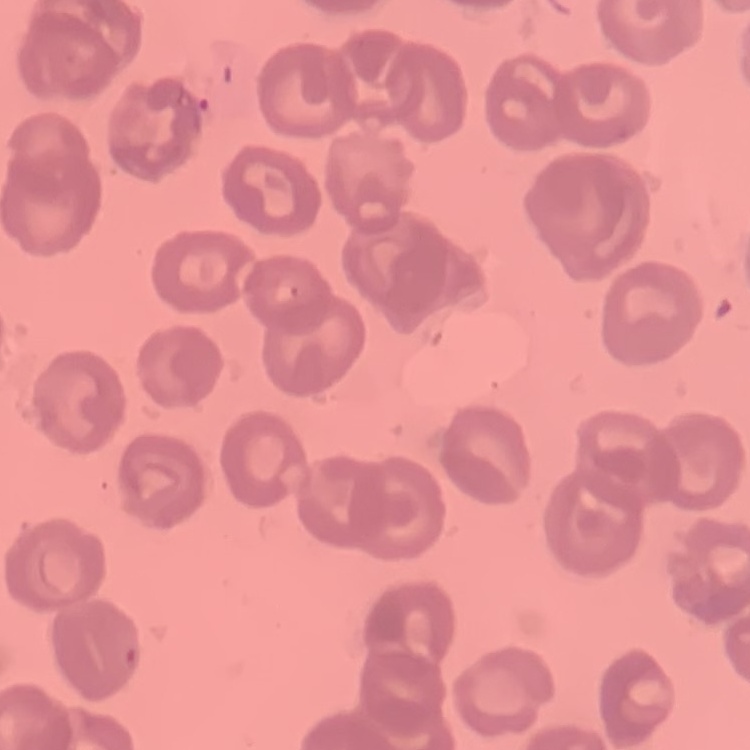

red blood cell morphology = no rouleaux formation
preparation = thin blood film
stain = Field's or Giemsa
image type = one tile cut from a larger photomicrograph